Report the malaria status of this cell.
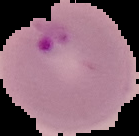

It is parasitized.

{
  "preparation": "thin blood film",
  "image_size": "139×136 pixels",
  "image_type": "segmented cell region on a black background"
}